Name the parasite shown.
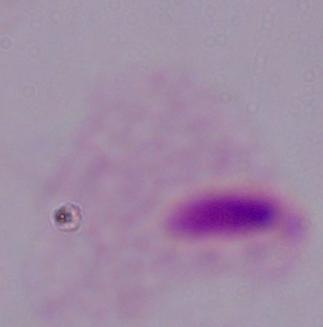
This is a trichomonad.

Micrograph. 1000x magnification.